Classify this cell by malaria status.
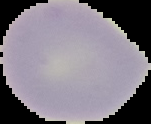

It is uninfected.

Summary:
  - Image size: 151×124 pixels
  - Image type: segmented cell region with the area outside set to black
  - Preparation: thin blood smear